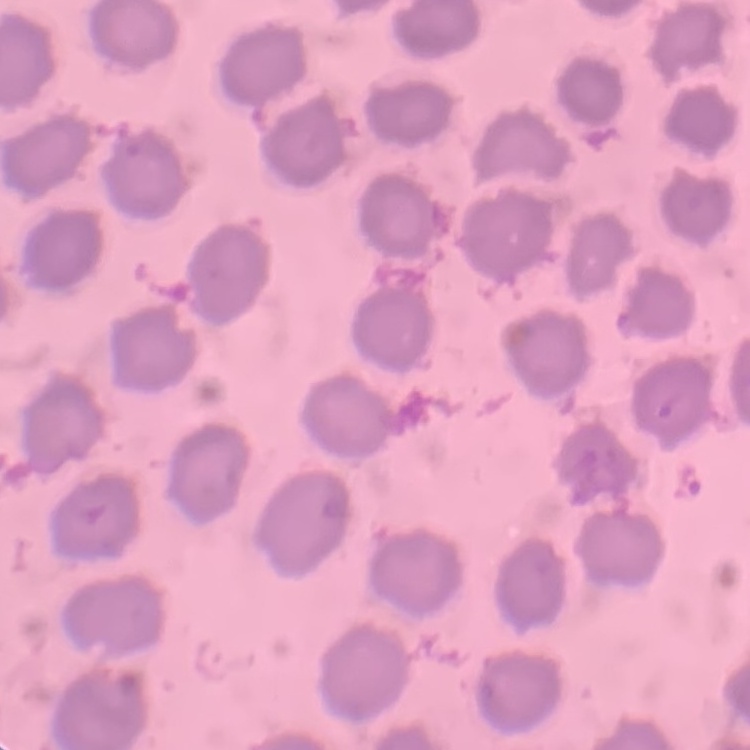
The red blood cells show no rouleaux formation. Thin blood smear. Field's or Giemsa stain. Square crop of a larger photomicrograph.